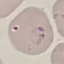

malaria status = parasitized
stain = Giemsa
preparation = thin smear
capture = smartphone camera at the microscope eyepiece
image type = cell patch, automatically extracted from a larger field of view and resized to 64 × 64 pixels